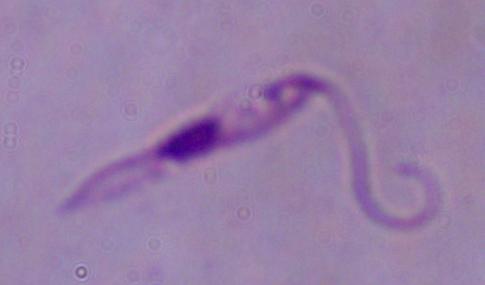

magnification = 1000x
modality = photomicrograph
identification = Leishmania